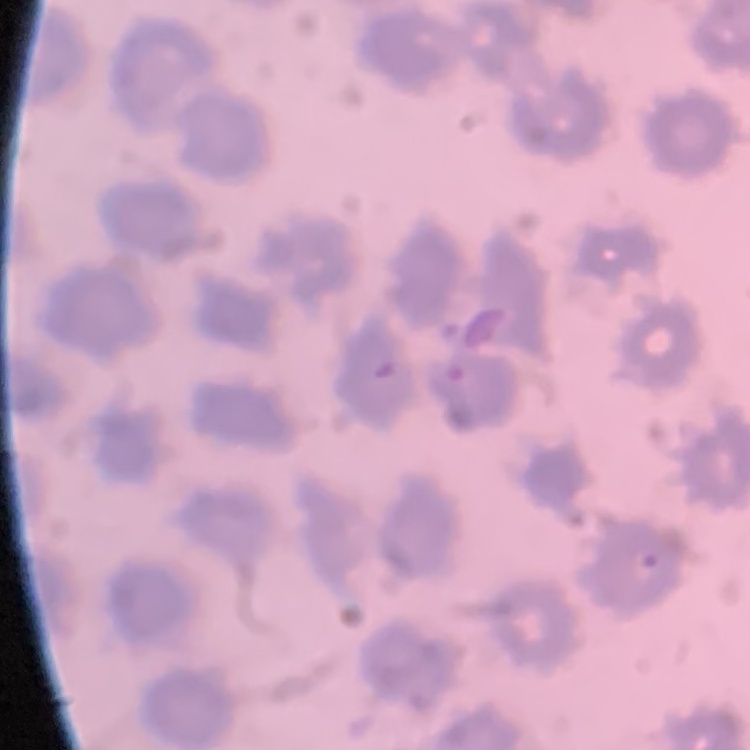
Summary:
  - Erythrocyte morphology: no rouleaux formation
  - Image type: one tile cut from a larger photomicrograph
  - Preparation: thin blood smear
  - Stain: Field's or Giemsa